Report the malaria status of this cell.
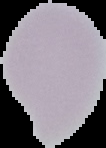
Uninfected.

Summary:
  - Image size: 106×148 pixels
  - Preparation: thin blood film
  - Image type: segmented cell region on a black background